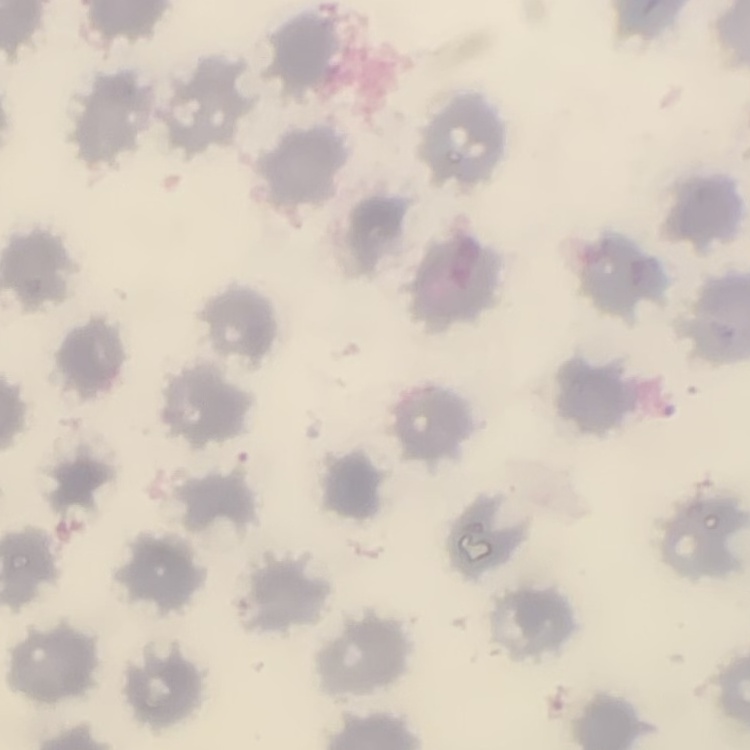

red blood cell morphology = no rouleaux formation
image type = square crop of a larger photomicrograph
preparation = thin blood smear
stain = Field's or Giemsa